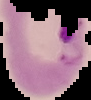

{
  "preparation": "thin blood film",
  "result": "Plasmodium parasites detected",
  "image_size": "91×100 pixels",
  "image_type": "segmented cell region on a black background"
}